Report the malaria status of this cell.
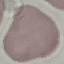
It is uninfected.

Summary:
  - Capture: smartphone through the microscope eyepiece
  - Stain: Giemsa
  - Image type: cell patch, automatically extracted from a larger field of view and resized to 64 × 64 pixels
  - Preparation: thin blood film